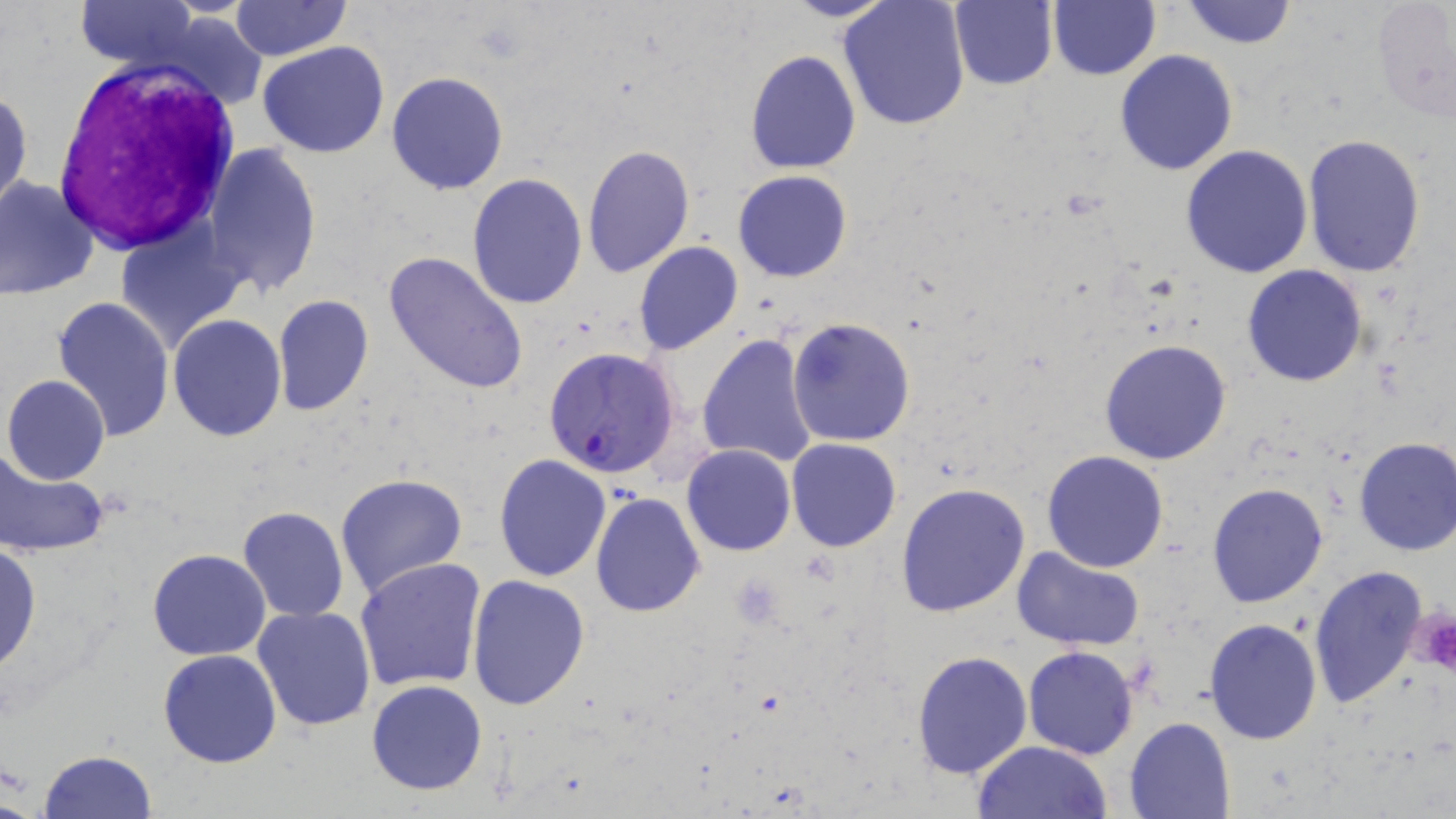
slide_level_diagnosis: Plasmodium falciparum
modality: light microscopy
uninfected_red_blood_cell_locations: 'approximate bounding boxes as (x1, y1, x2, y2) in pixels: (232, 0, 348, 59), (784, 0, 897, 21), (1181, 0, 1297, 48), (1371, 0, 1455, 122), (77, 1, 197, 73), (838, 1, 970, 131), (947, 1, 1058, 90), (1048, 2, 1161, 80), (258, 41, 389, 158), (745, 48, 860, 173), (1114, 49, 1238, 176), (386, 71, 508, 193), (0, 85, 33, 219), (1302, 135, 1427, 277), (203, 141, 321, 298), (581, 144, 695, 279), (1181, 146, 1313, 280), (733, 170, 852, 282), (466, 172, 589, 309), (0, 176, 99, 301), (114, 220, 246, 353), (633, 241, 743, 355), (383, 250, 530, 395), (1242, 264, 1367, 387), (273, 294, 373, 416), (53, 296, 174, 442), (168, 315, 287, 442), (786, 316, 915, 446), (696, 333, 820, 468), (1099, 339, 1232, 466), (2, 374, 110, 486), (1352, 436, 1456, 556), (786, 438, 902, 552), (682, 444, 795, 556), (0, 448, 110, 561), (1042, 451, 1168, 573), (494, 454, 613, 581), (335, 472, 469, 598), (897, 482, 1031, 617), (1206, 483, 1328, 608), (590, 491, 706, 616), (238, 506, 349, 623), (0, 543, 41, 674), (148, 549, 271, 660), (1013, 549, 1144, 650), (355, 556, 488, 692), (1309, 565, 1430, 710), (466, 574, 592, 710), (252, 605, 375, 732), (1204, 617, 1322, 744), (1022, 645, 1139, 759), (157, 649, 283, 768), (910, 650, 1032, 778), (367, 679, 488, 796), (1124, 717, 1234, 818), (973, 740, 1112, 819), (38, 748, 158, 818)'
platelet_locations: 'approximate bounding boxes as (x1, y1, x2, y2) in pixels: (1409, 610, 1456, 675)'
field_of_view: single
stain: May-Grünwald-Giemsa
plasmodium_falciparum_infected_red_blood_cell_locations: 'approximate bounding boxes as (x1, y1, x2, y2) in pixels: (542, 346, 680, 478)'
image_size: 1456×819 pixels
white_blood_cell_locations: 'approximate bounding boxes as (x1, y1, x2, y2) in pixels: (52, 64, 243, 246)'
preparation: thin blood smear
magnification: 1000x